Locate every Plasmodium parasite by life-cycle stage, and every leukocyte.
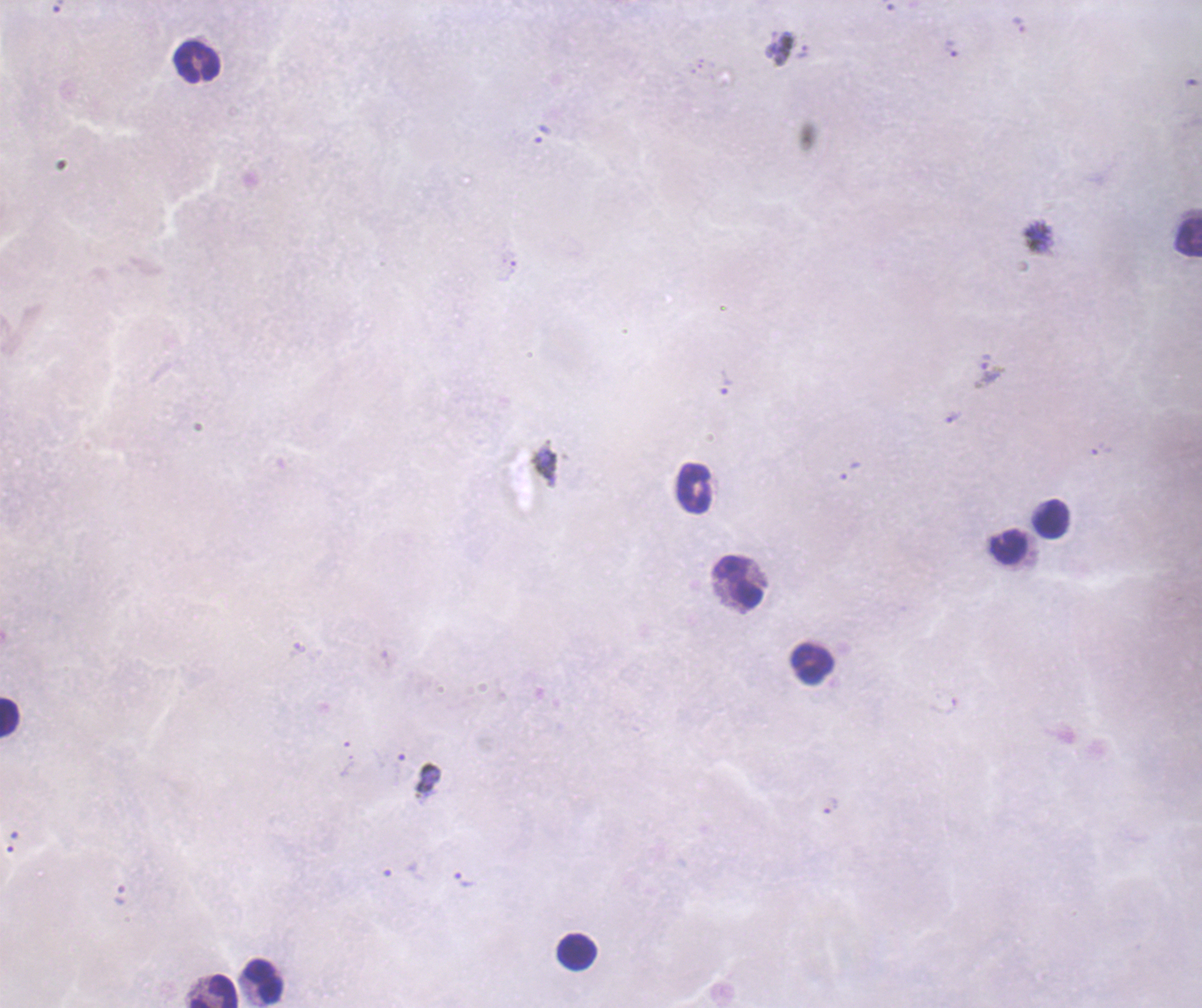

Approximate object centers, in pixels from the top-left corner.
Trophozoites: (x=1019, y=25), (x=951, y=48), (x=803, y=51), (x=989, y=371), (x=727, y=383), (x=953, y=417), (x=1101, y=449), (x=850, y=472), (x=830, y=806), (x=12, y=842), (x=465, y=881).
No schizont or gametocyte forms observed.
Leukocytes: (x=198, y=62), (x=1189, y=236), (x=693, y=488), (x=1050, y=519), (x=1007, y=547), (x=739, y=582), (x=811, y=663), (x=9, y=716), (x=576, y=950), (x=263, y=981), (x=213, y=991).

Summary:
  - Magnification: 100x
  - Stain: Romanowsky
  - Background quality: poor
  - Preparation: thick blood smear
  - Field of view: one from this slide
  - Coloration quality: bad
  - Image size: 1202×1008 pixels
  - Context: previously used in a real diagnosis